Outline platelets.
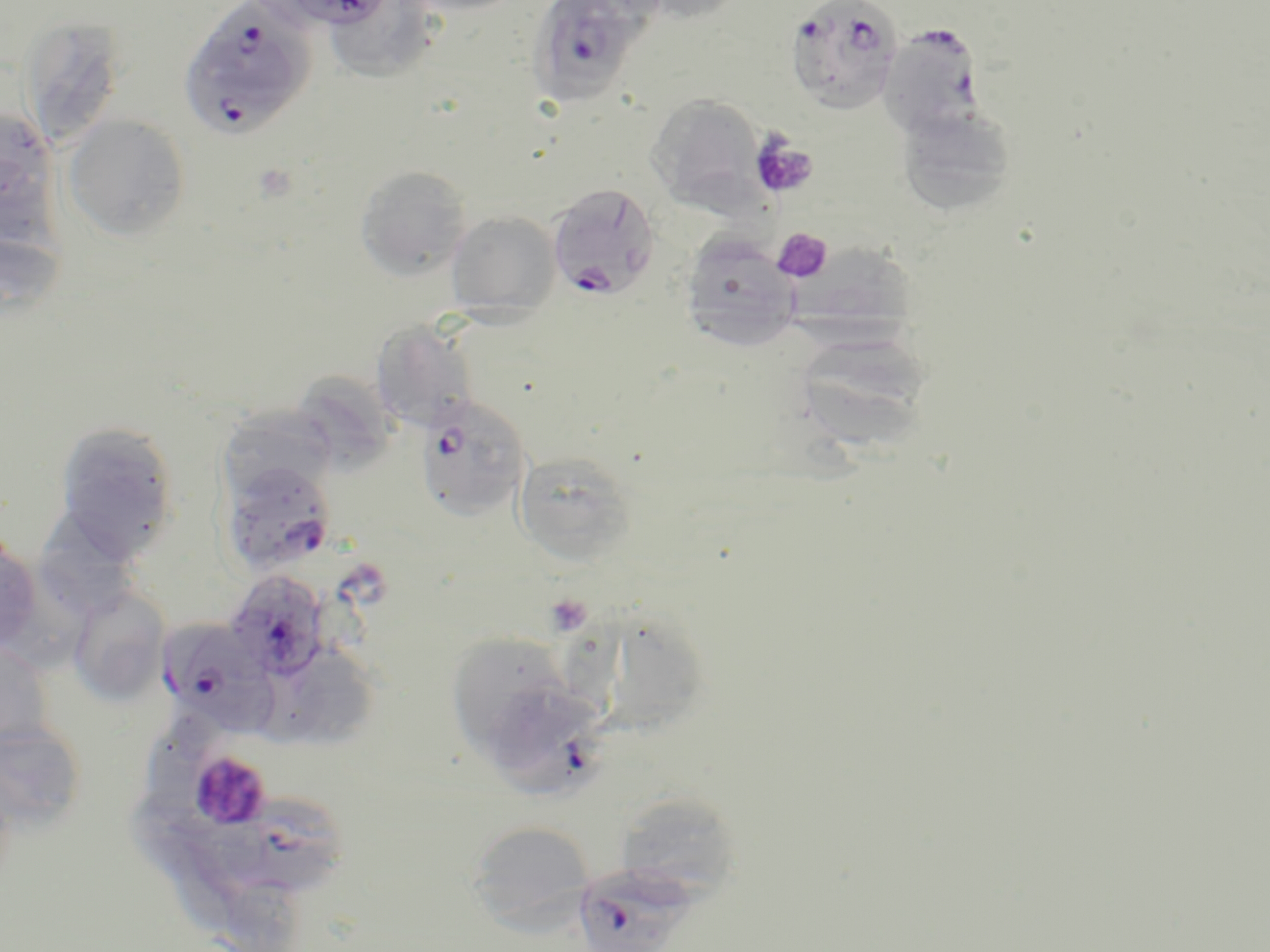
Approximate bounding boxes as named x1/y1/x2/y2 corners in pixels.
Platelets: (x1=750, y1=135, x2=817, y2=199), (x1=251, y1=161, x2=299, y2=204), (x1=772, y1=228, x2=833, y2=282), (x1=546, y1=594, x2=592, y2=634), (x1=188, y1=749, x2=272, y2=831).

Plasmodium falciparum-infected red blood cell locations: (x1=178, y1=0, x2=317, y2=140), (x1=254, y1=0, x2=396, y2=32), (x1=525, y1=0, x2=660, y2=107), (x1=785, y1=1, x2=904, y2=115), (x1=878, y1=24, x2=986, y2=140), (x1=547, y1=183, x2=661, y2=300), (x1=415, y1=394, x2=532, y2=522), (x1=220, y1=461, x2=338, y2=576), (x1=225, y1=570, x2=330, y2=682), (x1=157, y1=616, x2=279, y2=733), (x1=500, y1=687, x2=608, y2=802), (x1=214, y1=801, x2=349, y2=899), (x1=573, y1=864, x2=696, y2=952). Uninfected red blood cell locations: (x1=400, y1=0, x2=528, y2=15), (x1=624, y1=0, x2=753, y2=25), (x1=334, y1=2, x2=434, y2=87), (x1=19, y1=16, x2=126, y2=148), (x1=646, y1=95, x2=766, y2=212), (x1=896, y1=104, x2=1018, y2=217), (x1=1, y1=108, x2=52, y2=207), (x1=63, y1=114, x2=190, y2=240), (x1=355, y1=165, x2=472, y2=280), (x1=0, y1=195, x2=65, y2=310), (x1=446, y1=212, x2=562, y2=317), (x1=679, y1=234, x2=802, y2=351), (x1=788, y1=240, x2=917, y2=352), (x1=370, y1=320, x2=480, y2=433), (x1=791, y1=329, x2=934, y2=450), (x1=293, y1=375, x2=408, y2=481), (x1=218, y1=407, x2=337, y2=499), (x1=53, y1=421, x2=180, y2=561), (x1=512, y1=450, x2=638, y2=565), (x1=48, y1=515, x2=142, y2=624), (x1=0, y1=538, x2=43, y2=657), (x1=68, y1=586, x2=171, y2=706), (x1=568, y1=624, x2=705, y2=741), (x1=443, y1=629, x2=562, y2=750), (x1=0, y1=642, x2=55, y2=751), (x1=292, y1=647, x2=385, y2=745), (x1=147, y1=715, x2=225, y2=803), (x1=0, y1=722, x2=87, y2=833), (x1=610, y1=790, x2=741, y2=901), (x1=129, y1=795, x2=228, y2=887), (x1=467, y1=820, x2=595, y2=929), (x1=227, y1=880, x2=310, y2=952). Slide-level diagnosis: Plasmodium falciparum. Image is 1270×952 pixels. Single field of view. May-Grünwald-Giemsa stain. 1000x magnification. Optical microscopy. Thin blood film.